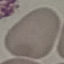

malaria status = uninfected
preparation = thin smear
stain = Giemsa
capture = smartphone through the microscope eyepiece
image type = cell patch, automatically extracted from a larger field of view and resized to 64 × 64 pixels